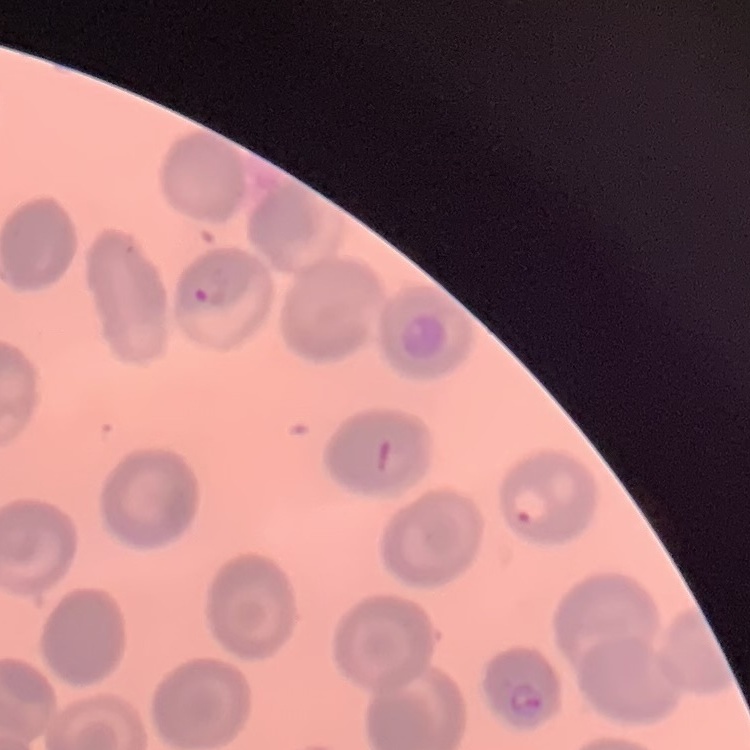
{
  "erythrocyte_morphology": "no rouleaux formation",
  "stain": "Field's or Giemsa",
  "preparation": "thin peripheral smear",
  "image_type": "square crop of a larger photomicrograph"
}